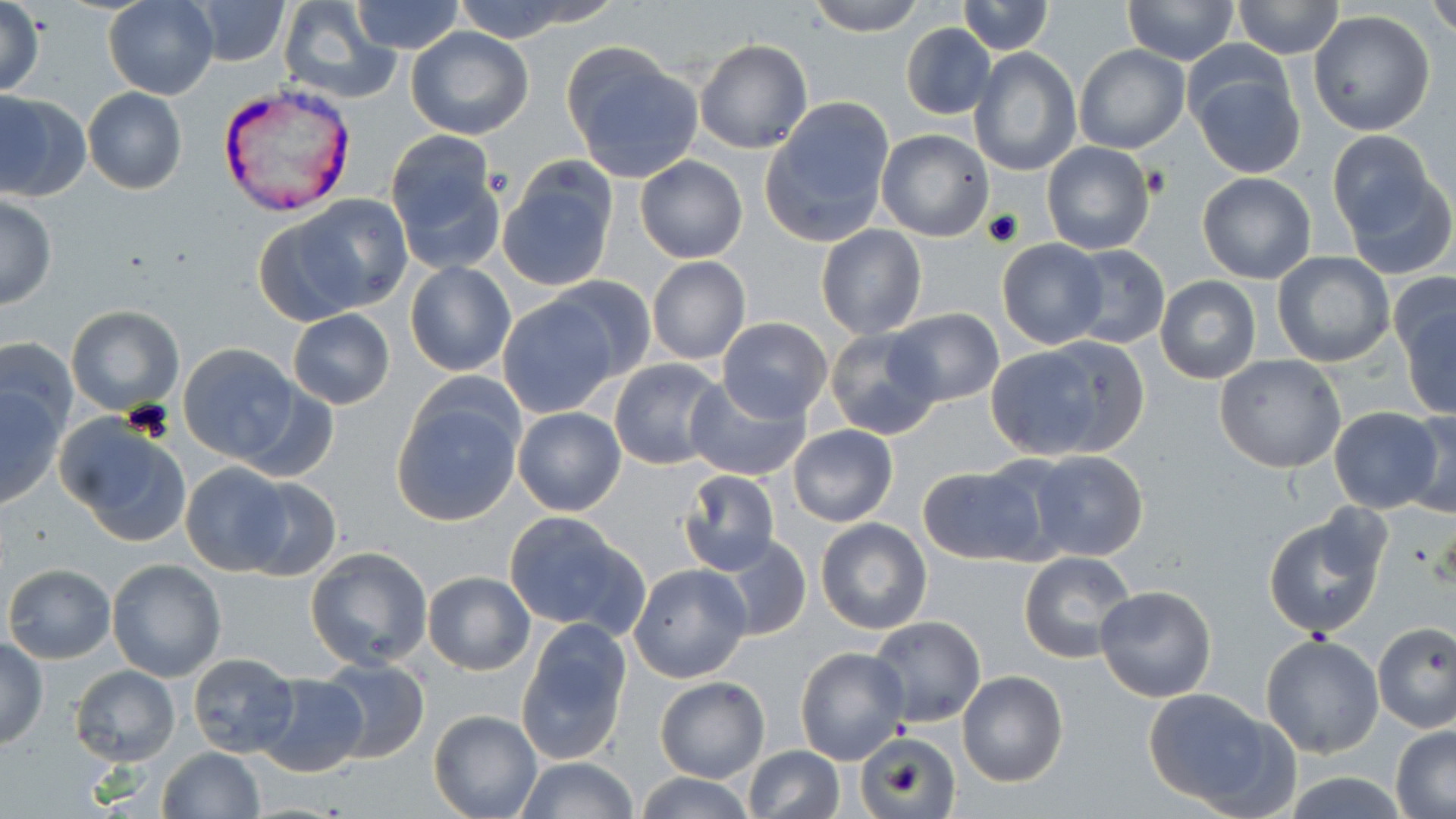

Summary:
  - Coordinate format: approximate bounding boxes as named x1/y1/x2/y2 corners in pixels
  - Uninfected red blood cell locations: (x1=103, y1=0, x2=218, y2=99), (x1=185, y1=0, x2=291, y2=66), (x1=276, y1=0, x2=399, y2=104), (x1=351, y1=0, x2=465, y2=55), (x1=450, y1=0, x2=598, y2=43), (x1=807, y1=0, x2=927, y2=34), (x1=956, y1=0, x2=1053, y2=54), (x1=1121, y1=0, x2=1239, y2=65), (x1=1232, y1=0, x2=1345, y2=58), (x1=1428, y1=0, x2=1456, y2=36), (x1=0, y1=3, x2=47, y2=98), (x1=909, y1=6, x2=1027, y2=88), (x1=1308, y1=10, x2=1437, y2=137), (x1=901, y1=22, x2=996, y2=119), (x1=405, y1=26, x2=533, y2=140), (x1=694, y1=37, x2=812, y2=153), (x1=1073, y1=44, x2=1190, y2=154), (x1=562, y1=45, x2=704, y2=183), (x1=969, y1=48, x2=1083, y2=177), (x1=1188, y1=57, x2=1307, y2=179), (x1=82, y1=88, x2=187, y2=194), (x1=0, y1=90, x2=91, y2=203), (x1=761, y1=99, x2=896, y2=247), (x1=876, y1=129, x2=995, y2=242), (x1=1327, y1=129, x2=1438, y2=239), (x1=383, y1=133, x2=506, y2=270), (x1=1041, y1=140, x2=1155, y2=255), (x1=635, y1=155, x2=747, y2=263), (x1=497, y1=161, x2=620, y2=290), (x1=1344, y1=169, x2=1455, y2=280), (x1=1197, y1=172, x2=1317, y2=283), (x1=0, y1=196, x2=57, y2=309), (x1=268, y1=197, x2=410, y2=321), (x1=815, y1=223, x2=927, y2=340), (x1=996, y1=239, x2=1109, y2=350), (x1=1065, y1=244, x2=1170, y2=350), (x1=1273, y1=253, x2=1395, y2=368), (x1=645, y1=256, x2=751, y2=365), (x1=404, y1=261, x2=517, y2=378), (x1=545, y1=273, x2=658, y2=384), (x1=1154, y1=276, x2=1261, y2=385), (x1=1395, y1=286, x2=1455, y2=419), (x1=495, y1=295, x2=620, y2=417), (x1=66, y1=304, x2=184, y2=415), (x1=886, y1=308, x2=1004, y2=408), (x1=288, y1=309, x2=395, y2=410), (x1=717, y1=319, x2=833, y2=420), (x1=825, y1=327, x2=944, y2=440), (x1=1039, y1=335, x2=1149, y2=456), (x1=1, y1=337, x2=78, y2=444), (x1=177, y1=343, x2=304, y2=464), (x1=984, y1=344, x2=1117, y2=460), (x1=1214, y1=354, x2=1348, y2=474), (x1=608, y1=357, x2=728, y2=469), (x1=685, y1=375, x2=812, y2=482), (x1=0, y1=380, x2=70, y2=509), (x1=237, y1=383, x2=338, y2=484), (x1=391, y1=389, x2=524, y2=528), (x1=1330, y1=406, x2=1442, y2=514), (x1=512, y1=407, x2=627, y2=516), (x1=1401, y1=409, x2=1456, y2=520), (x1=57, y1=416, x2=192, y2=545), (x1=788, y1=425, x2=897, y2=528), (x1=1022, y1=450, x2=1150, y2=562), (x1=179, y1=461, x2=297, y2=574), (x1=917, y1=466, x2=1044, y2=565), (x1=676, y1=470, x2=780, y2=576), (x1=232, y1=476, x2=342, y2=580), (x1=503, y1=510, x2=644, y2=638), (x1=1263, y1=512, x2=1387, y2=638), (x1=815, y1=518, x2=932, y2=635), (x1=712, y1=533, x2=812, y2=642), (x1=305, y1=546, x2=434, y2=670), (x1=1019, y1=551, x2=1136, y2=664), (x1=106, y1=558, x2=228, y2=681), (x1=4, y1=563, x2=115, y2=664), (x1=627, y1=563, x2=752, y2=684), (x1=423, y1=570, x2=536, y2=675), (x1=1095, y1=584, x2=1217, y2=701), (x1=867, y1=616, x2=985, y2=727), (x1=516, y1=621, x2=634, y2=765), (x1=1372, y1=621, x2=1456, y2=733), (x1=893, y1=632, x2=1024, y2=765), (x1=1260, y1=633, x2=1385, y2=757), (x1=0, y1=635, x2=48, y2=749), (x1=796, y1=646, x2=909, y2=764), (x1=186, y1=653, x2=299, y2=758), (x1=316, y1=658, x2=430, y2=765), (x1=70, y1=665, x2=180, y2=765), (x1=956, y1=670, x2=1068, y2=786), (x1=254, y1=673, x2=366, y2=778), (x1=655, y1=677, x2=770, y2=783), (x1=1141, y1=690, x2=1289, y2=815), (x1=429, y1=708, x2=541, y2=819), (x1=1390, y1=724, x2=1455, y2=817), (x1=861, y1=736, x2=951, y2=817), (x1=744, y1=746, x2=844, y2=818), (x1=158, y1=747, x2=265, y2=819), (x1=513, y1=757, x2=640, y2=817), (x1=1281, y1=769, x2=1411, y2=818), (x1=631, y1=774, x2=760, y2=818)
  - Plasmodium vivax-infected red blood cell locations: (x1=219, y1=84, x2=351, y2=217)
  - Platelet locations: (x1=1144, y1=167, x2=1171, y2=198)
  - Slide-level diagnosis: Plasmodium vivax
  - Image size: 1456×819 pixels
  - Stain: May-Grünwald-Giemsa
  - Field of view: one of a larger specimen
  - Magnification: 1000x
  - Modality: light microscopy
  - Preparation: thin blood film